Name the cell type shown.
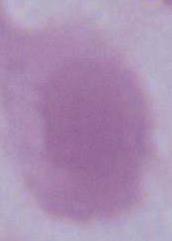

This is an erythrocyte.

Photomicrograph. Captured at 1000x magnification.